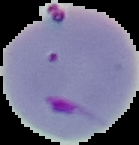 Image is 139×145 pixels. Cell region segmented out of the field of view; the surrounding area is masked to black. Result: Plasmodium parasites identified. From a thin blood film.